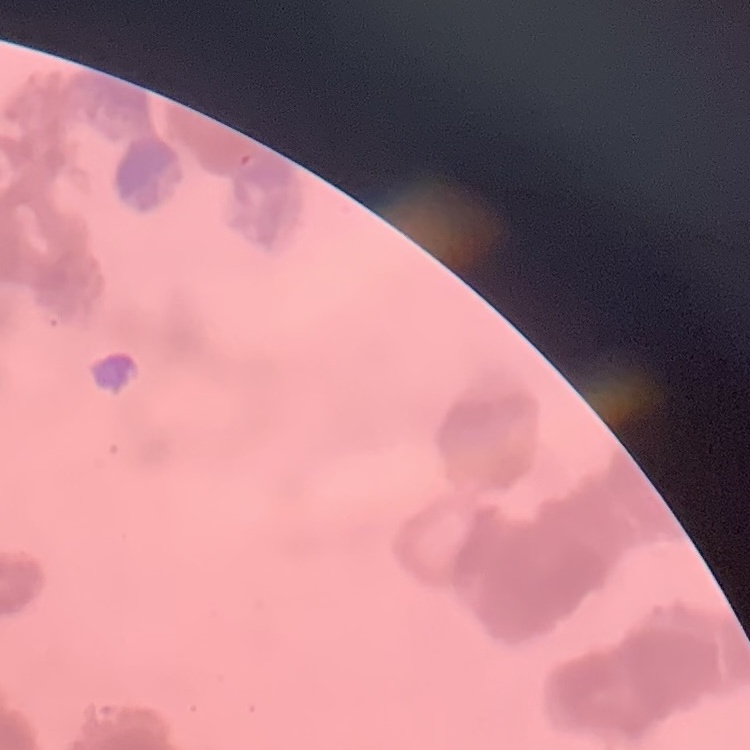
erythrocyte morphology = rouleaux formation
preparation = thin blood film
image type = one tile cut from a larger photomicrograph
stain = Field's or Giemsa